Report the malaria status of this cell.
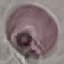
It is uninfected.

preparation = thin blood film
capture = smartphone through the microscope eyepiece
image type = cell patch, automatically extracted from a larger field of view and resized to 64 × 64 pixels
stain = Giemsa